State the blood parasite species.
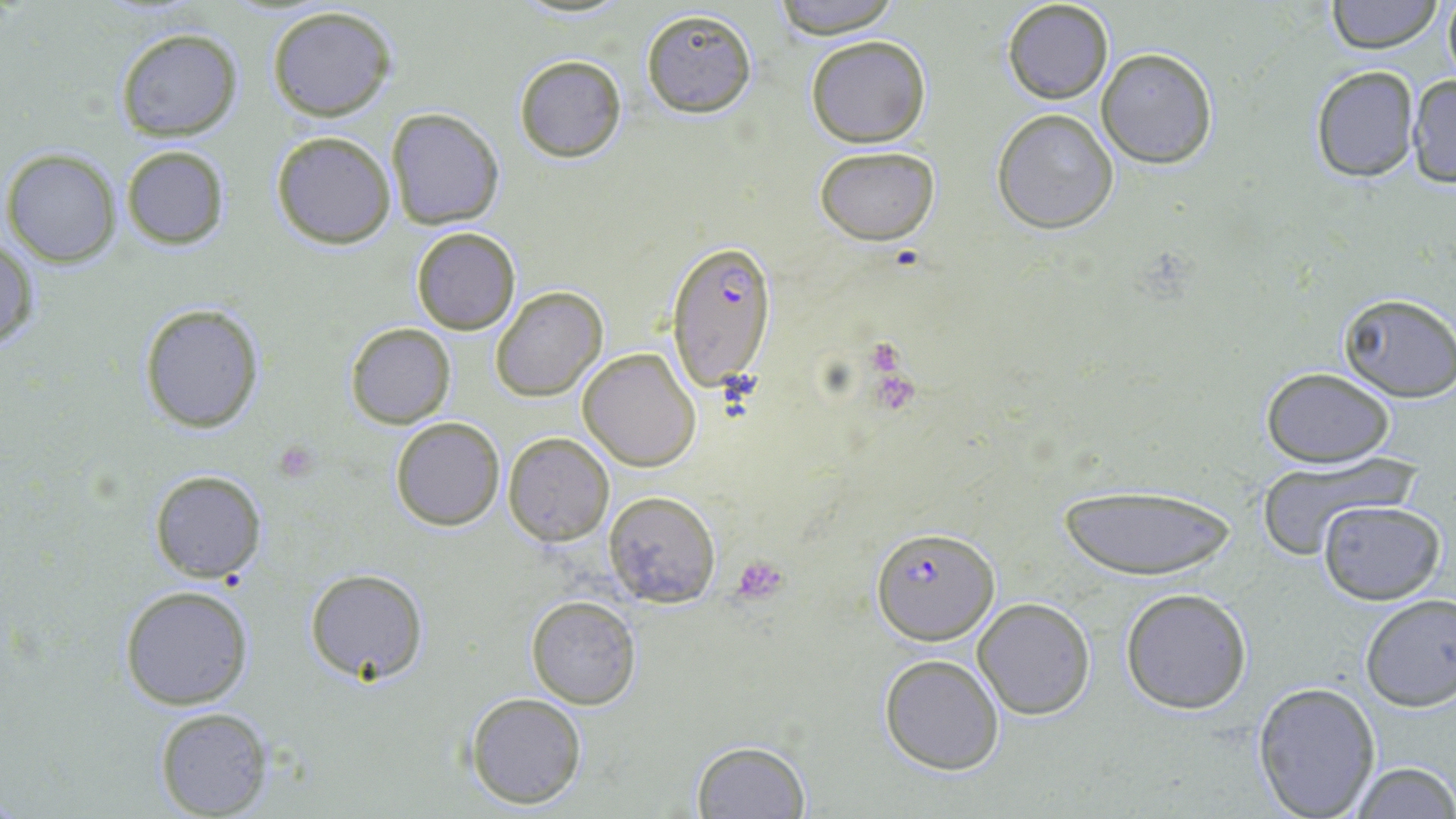
Plasmodium falciparum.

modality = light microscopy
uninfected red blood cell locations = approximate bounding boxes as (x1, y1, x2, y2) in pixels: (766, 0, 904, 39), (1002, 0, 1113, 105), (1326, 0, 1441, 53), (1442, 0, 1456, 81), (265, 4, 399, 121), (639, 9, 756, 118), (114, 26, 242, 141), (805, 35, 931, 148), (1096, 47, 1217, 169), (513, 55, 627, 163), (1309, 65, 1421, 183), (1405, 72, 1456, 188), (386, 108, 505, 228), (991, 109, 1119, 234), (271, 130, 397, 248), (120, 144, 230, 250), (814, 144, 940, 244), (3, 147, 122, 266), (410, 226, 521, 335), (0, 236, 38, 355), (491, 286, 606, 402), (1337, 292, 1456, 403), (139, 302, 266, 432), (344, 322, 457, 428), (578, 347, 701, 472), (1262, 368, 1395, 467), (390, 418, 504, 531), (503, 432, 614, 545), (1254, 453, 1417, 558), (149, 470, 266, 582), (1055, 482, 1238, 581), (603, 492, 720, 607), (1317, 499, 1446, 604), (304, 568, 427, 685), (118, 584, 253, 710), (1120, 588, 1252, 714), (1357, 593, 1456, 713), (527, 596, 641, 709), (973, 597, 1095, 719), (878, 654, 1005, 775), (1252, 681, 1381, 818), (464, 691, 588, 809), (153, 707, 271, 817), (690, 740, 811, 818), (1347, 759, 1455, 819)
platelet locations = approximate bounding boxes as (x1, y1, x2, y2) in pixels: (731, 556, 787, 603)
preparation = thin blood film
field of view = single
stain = May-Grünwald-Giemsa
magnification = 1000x
Plasmodium falciparum-infected red blood cell locations = approximate bounding boxes as (x1, y1, x2, y2) in pixels: (664, 240, 778, 391), (873, 527, 998, 643)
image size = 1456×819 pixels